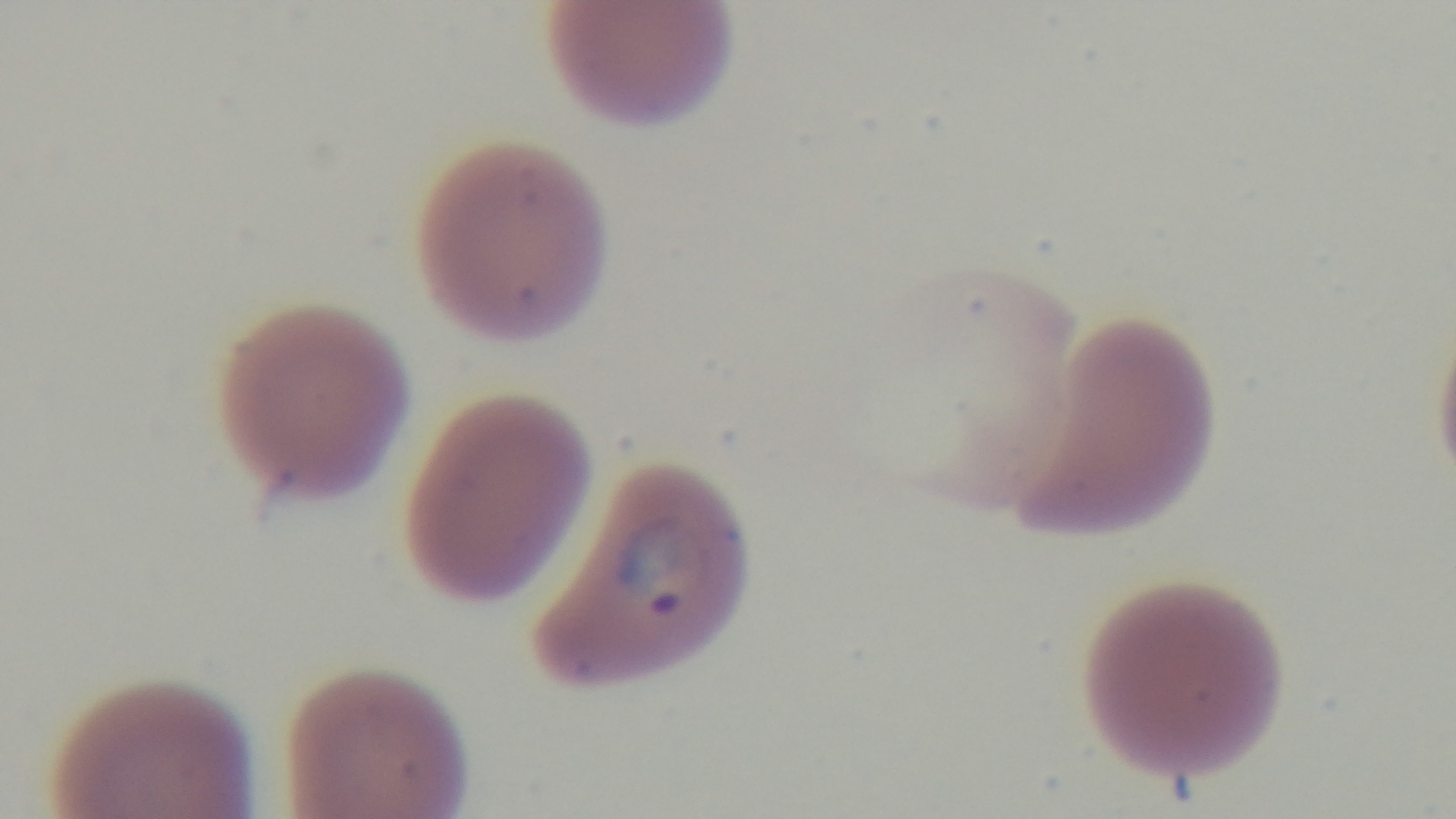

Summary:
  - Field of view: single
  - Capture: mounted 4K digital camera
  - Preparation: thin
  - Malaria status: positive
  - Objective: 100x oil immersion
  - Stain: Giemsa
  - Modality: light microscopy